Locate and identify every blood parasite.
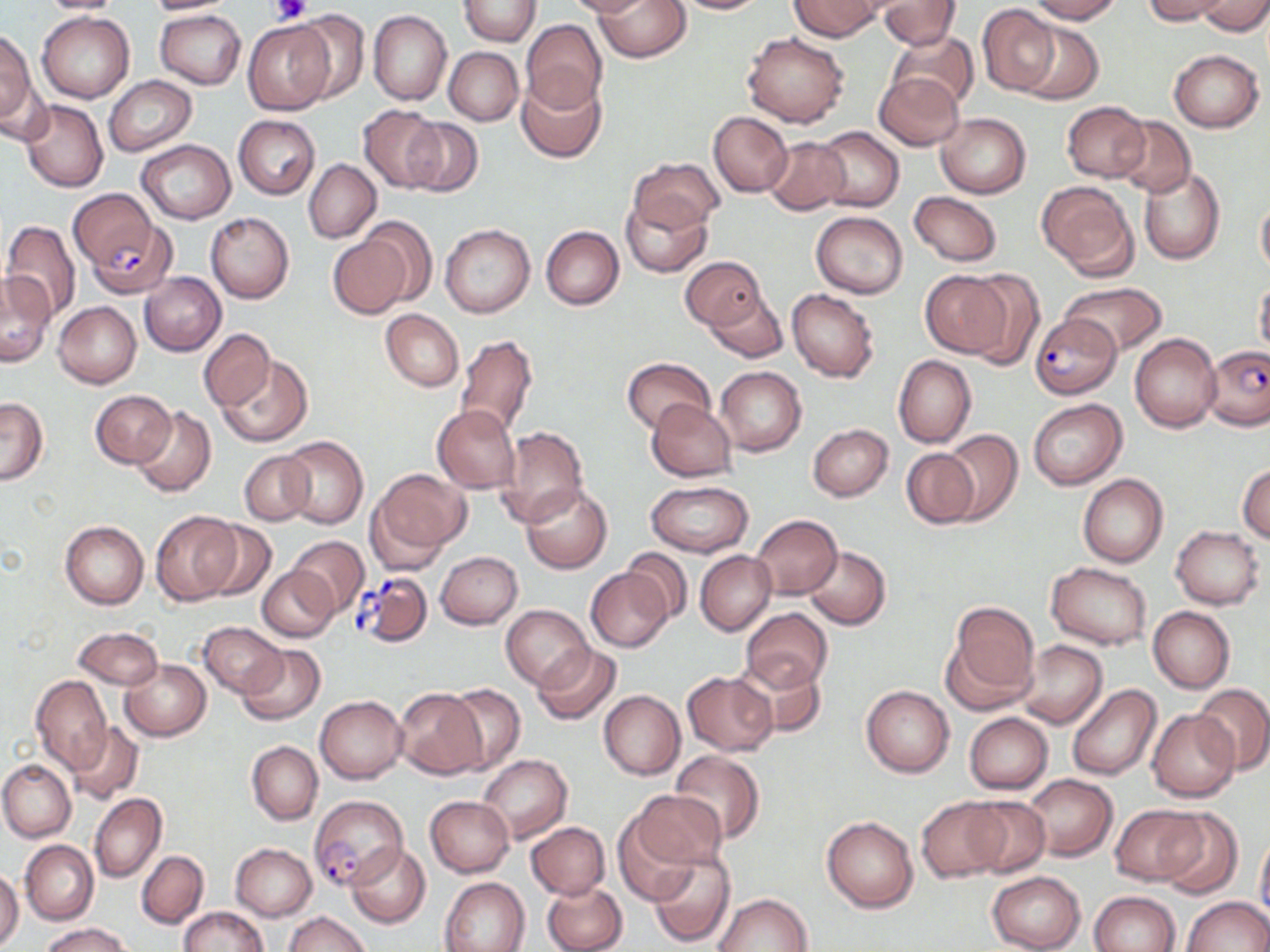

Approximate bounding boxes as (x1,y1)-(x2,y2) corner pairs in pixels.
Plasmodium falciparum-infected red blood cells: (68,187)-(182,299), (1031,312)-(1121,398), (1203,344)-(1270,431), (352,569)-(433,647), (309,796)-(408,892).
No Plasmodium ovale, Plasmodium malariae, Plasmodium vivax, Babesia divergens, or Trypanosoma brucei observed.

Summary:
  - Platelet locations: (271,0)-(311,26)
  - Uninfected red blood cell locations: (36,0)-(131,15), (143,0)-(236,14), (457,0)-(540,46), (564,0)-(655,17), (594,0)-(691,62), (666,0)-(771,14), (787,0)-(884,40), (873,0)-(961,50), (1023,0)-(1125,23), (1141,0)-(1233,24), (1197,1)-(1270,36), (978,4)-(1060,96), (155,9)-(246,89), (290,9)-(371,105), (37,11)-(135,103), (368,11)-(451,105), (521,19)-(607,112), (244,20)-(333,114), (1017,21)-(1102,104), (0,28)-(36,129), (742,32)-(850,128), (886,32)-(979,113), (444,47)-(524,125), (1168,49)-(1264,132), (874,72)-(964,150), (516,74)-(608,164), (103,76)-(198,156), (0,77)-(54,145), (21,99)-(107,193), (1062,101)-(1150,182), (359,105)-(446,193), (709,111)-(793,197), (936,112)-(1030,198), (233,115)-(319,199), (1113,115)-(1195,198), (404,120)-(484,197), (814,127)-(904,211), (763,136)-(851,215), (137,140)-(235,223), (629,156)-(723,232), (304,159)-(381,242), (1137,167)-(1227,266), (1037,180)-(1138,279), (908,191)-(1004,267), (621,195)-(712,278), (1256,195)-(1270,281), (811,211)-(908,298), (206,212)-(294,303), (364,217)-(438,306), (1,220)-(81,324), (439,223)-(535,317), (541,226)-(624,310), (326,232)-(413,319), (680,256)-(766,329), (961,269)-(1046,369), (920,270)-(1012,357), (139,272)-(227,355), (0,273)-(56,366), (1255,279)-(1270,362), (1058,282)-(1167,356), (703,289)-(788,363), (787,289)-(879,382), (54,302)-(141,388), (380,310)-(463,392), (199,329)-(274,410), (1130,332)-(1221,433), (456,334)-(537,437), (216,354)-(313,447), (893,355)-(975,448), (622,357)-(714,434), (714,367)-(807,454), (90,390)-(176,469), (0,397)-(48,485), (1027,399)-(1126,488), (648,400)-(737,481), (130,405)-(217,497), (433,405)-(521,493), (807,424)-(893,500), (497,427)-(588,526), (940,430)-(1022,525), (280,436)-(368,529), (901,447)-(981,529), (239,451)-(314,526), (1238,464)-(1270,543), (368,470)-(468,564), (1078,474)-(1167,567), (645,481)-(754,557), (521,484)-(612,573), (151,512)-(241,604), (752,514)-(842,599), (199,519)-(276,601), (60,521)-(148,609), (1171,526)-(1263,609), (287,536)-(370,617), (803,545)-(891,629), (623,548)-(693,623), (436,551)-(522,629), (695,551)-(775,635), (1046,562)-(1152,650), (257,565)-(337,642), (585,567)-(674,652), (942,601)-(1040,712), (501,604)-(593,690), (1148,606)-(1235,693), (741,608)-(834,692), (199,623)-(287,697), (72,627)-(163,690), (1017,640)-(1107,728), (532,643)-(621,726), (238,645)-(326,726), (734,655)-(826,739), (120,659)-(211,741), (682,670)-(777,756), (30,676)-(112,772), (442,684)-(525,774), (861,684)-(954,777), (1066,684)-(1161,780), (1193,684)-(1270,774), (393,687)-(485,779), (598,690)-(685,780), (316,695)-(406,784), (1148,709)-(1239,802), (963,712)-(1054,794), (65,722)-(144,804), (247,741)-(323,825), (670,751)-(765,843), (477,753)-(571,843), (0,759)-(75,842), (1022,774)-(1118,861), (628,788)-(728,872), (89,793)-(166,882), (425,796)-(514,876), (964,796)-(1051,876), (917,797)-(1009,881), (1111,804)-(1206,884), (1156,810)-(1243,897), (821,814)-(918,913), (613,817)-(701,907), (526,822)-(610,900), (1255,829)-(1270,923), (20,841)-(98,924), (231,843)-(317,920), (346,843)-(432,928), (136,850)-(209,928), (648,850)-(735,948), (0,867)-(23,949), (985,870)-(1086,952), (440,876)-(531,952), (542,879)-(626,952), (1091,891)-(1181,952), (714,892)-(813,951), (1181,896)-(1269,952), (180,906)-(268,952), (284,911)-(369,952), (40,923)-(132,952)
  - Slide-level diagnosis: Plasmodium falciparum
  - Field of view: one of a larger specimen
  - Preparation: thin blood smear
  - Modality: optical microscopy
  - Image size: 1270×952 pixels
  - Magnification: 1000x
  - Stain: May-Grünwald-Giemsa